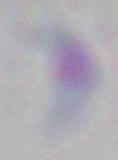
modality = photomicrograph
identification = Toxoplasma gondii
magnification = 1000x